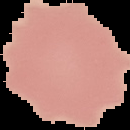
Summary:
  - Result: no malaria parasites seen
  - Image type: segmented cell region on a black background
  - Image size: 130×130 pixels
  - Preparation: thin blood film